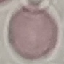
Summary:
  - Result: no malaria parasites seen
  - Preparation: thin smear
  - Stain: Giemsa
  - Capture: smartphone camera at the microscope eyepiece
  - Image type: cell patch, automatically extracted from a larger field of view and resized to 64 × 64 pixels